Assess this cell for malaria.
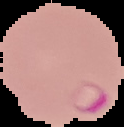
It is parasitized.

image type = cell region segmented out of the field of view; surrounding area masked to black
preparation = thin blood smear
image size = 124×127 pixels